Give the extent of all uninfected red blood cells.
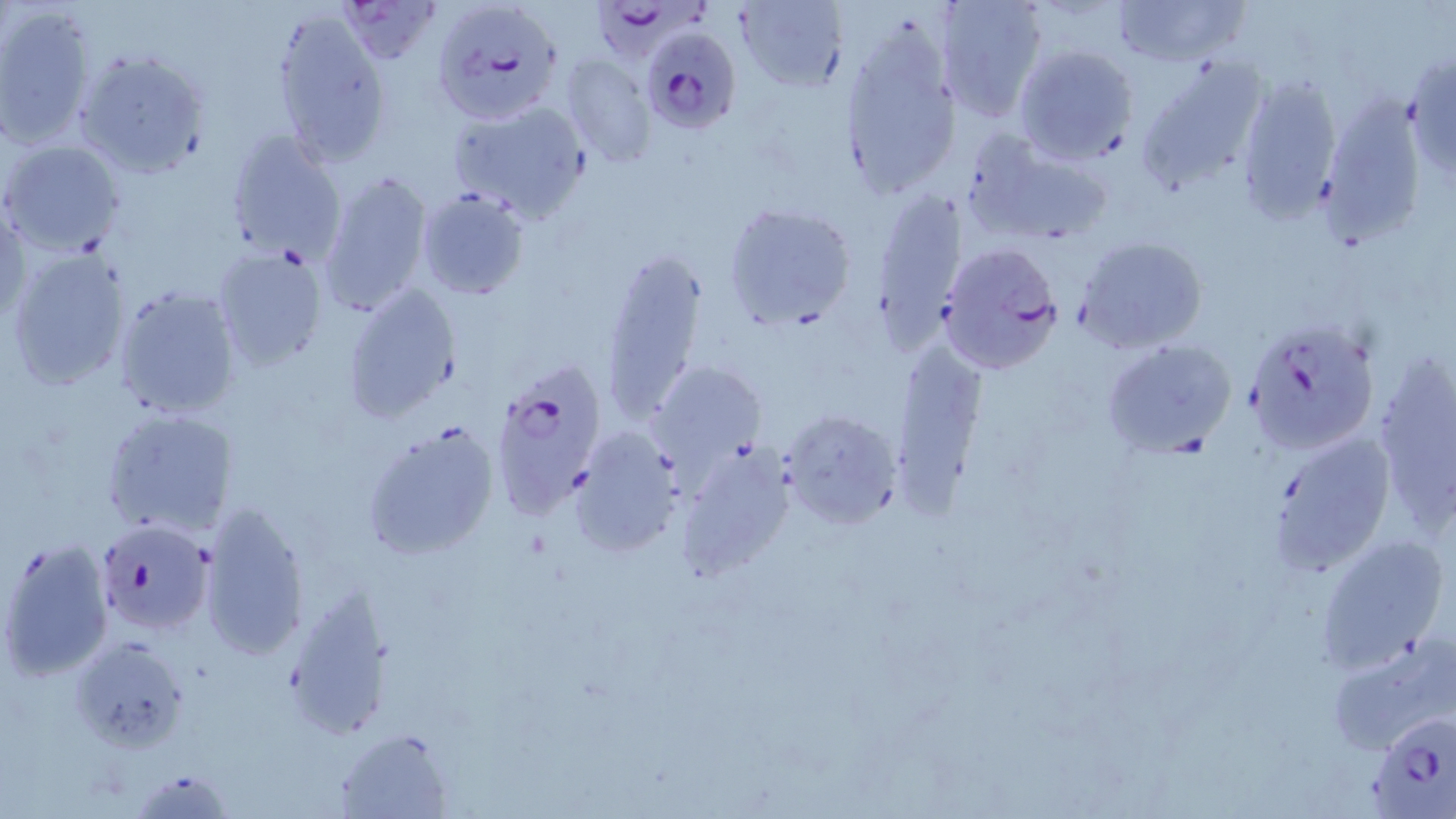
Approximate bounding boxes as [x1, y1, x2, y2] in pixels.
Uninfected red blood cells: [339, 0, 441, 65], [935, 0, 1047, 122], [1111, 0, 1246, 67], [734, 1, 845, 91], [0, 5, 97, 149], [272, 12, 392, 162], [838, 21, 960, 200], [1012, 44, 1139, 165], [72, 48, 212, 179], [1135, 49, 1271, 190], [1405, 49, 1455, 179], [559, 54, 658, 167], [1236, 73, 1344, 222], [1320, 95, 1425, 244], [445, 97, 592, 224], [224, 129, 347, 263], [963, 133, 1113, 245], [2, 138, 127, 256], [318, 168, 436, 318], [415, 186, 530, 301], [870, 188, 968, 337], [1, 194, 29, 327], [723, 200, 858, 333], [1075, 235, 1209, 353], [4, 245, 134, 393], [212, 245, 332, 371], [598, 247, 708, 425], [341, 281, 463, 423], [112, 284, 242, 420], [1100, 337, 1238, 460], [889, 340, 984, 504], [1370, 355, 1456, 525], [646, 359, 768, 476], [651, 381, 781, 549], [101, 406, 233, 540], [779, 407, 904, 531], [361, 420, 499, 561], [572, 429, 683, 555], [1266, 429, 1397, 577], [677, 444, 799, 580], [197, 499, 310, 662], [1313, 534, 1451, 670], [2, 538, 114, 680], [282, 587, 391, 743], [1326, 629, 1456, 753], [70, 635, 192, 752], [335, 727, 453, 817].

Plasmodium falciparum-infected red blood cell locations: [430, 0, 561, 126], [597, 0, 715, 71], [643, 28, 740, 132], [935, 240, 1061, 375], [1243, 320, 1379, 456], [485, 358, 611, 523], [93, 519, 215, 637], [1367, 707, 1455, 818]. Slide-level diagnosis: Plasmodium falciparum. Thin blood film. Image is 1456×819 pixels. 1000x magnification. Light microscopy. One field of a larger specimen. May-Grünwald-Giemsa-stained preparation.